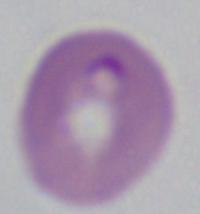

magnification = 1000x
identification = Babesia
modality = micrograph